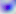
{
  "identification": "Toxoplasma gondii",
  "modality": "micrograph",
  "magnification": "400x"
}